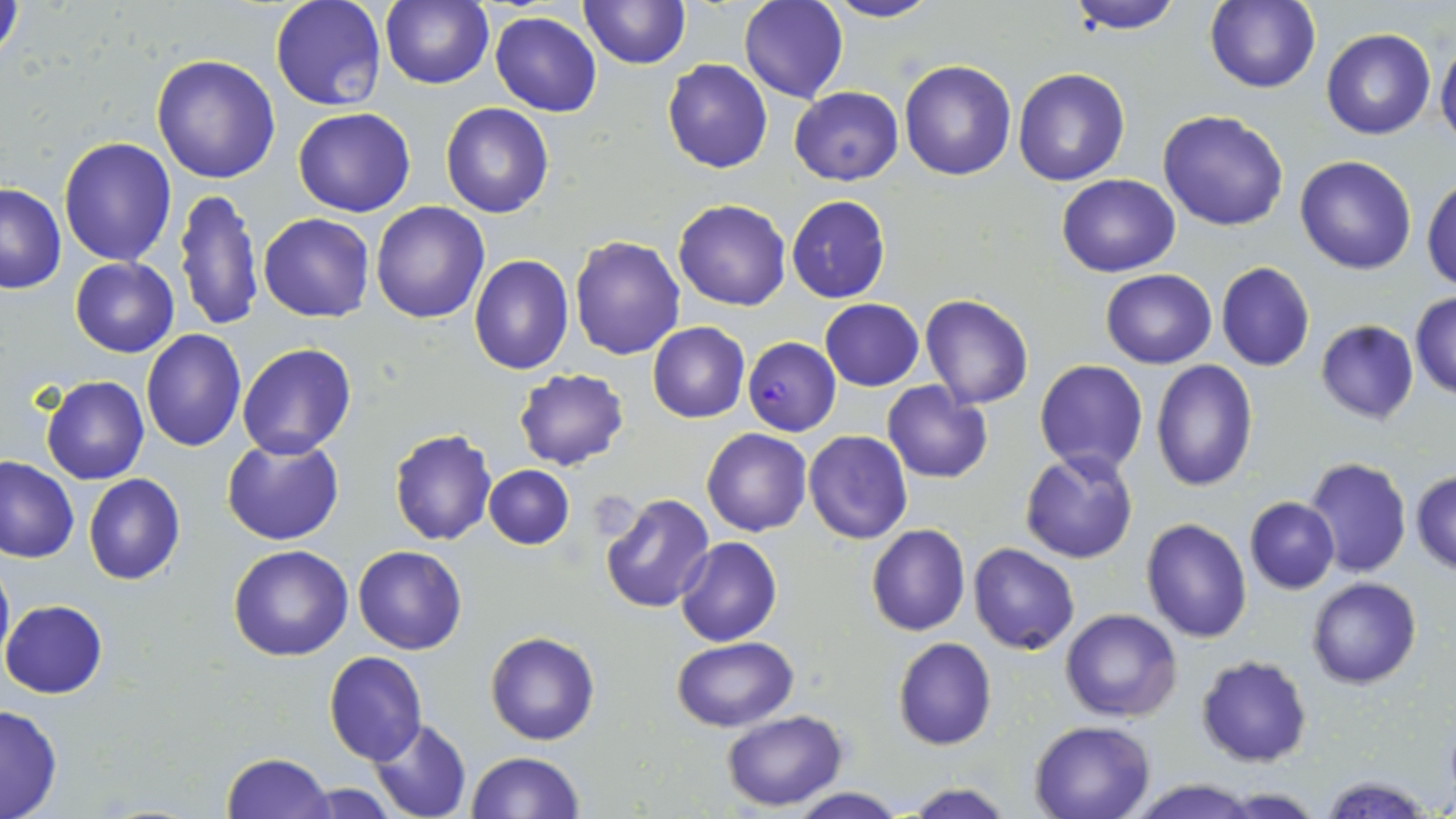
Plasmodium falciparum-infected red blood cell locations = approximate bounding boxes as named x1/y1/x2/y2 corners in pixels: (x1=744, y1=337, x2=842, y2=436)
slide-level diagnosis = Plasmodium falciparum
image size = 1456×819 pixels
field of view = one of a larger specimen
uninfected red blood cell locations = approximate bounding boxes as named x1/y1/x2/y2 corners in pixels: (x1=382, y1=0, x2=494, y2=89), (x1=580, y1=0, x2=691, y2=70), (x1=824, y1=0, x2=940, y2=24), (x1=1064, y1=0, x2=1188, y2=32), (x1=272, y1=1, x2=386, y2=112), (x1=738, y1=1, x2=848, y2=104), (x1=1204, y1=1, x2=1321, y2=93), (x1=1, y1=2, x2=28, y2=68), (x1=491, y1=10, x2=603, y2=117), (x1=1321, y1=29, x2=1435, y2=140), (x1=1435, y1=39, x2=1456, y2=149), (x1=151, y1=55, x2=281, y2=185), (x1=662, y1=58, x2=772, y2=174), (x1=898, y1=60, x2=1017, y2=181), (x1=1013, y1=67, x2=1130, y2=185), (x1=788, y1=86, x2=904, y2=185), (x1=440, y1=102, x2=554, y2=218), (x1=293, y1=105, x2=416, y2=218), (x1=1158, y1=109, x2=1290, y2=231), (x1=59, y1=136, x2=177, y2=266), (x1=1294, y1=155, x2=1417, y2=274), (x1=1056, y1=173, x2=1180, y2=275), (x1=1422, y1=175, x2=1456, y2=291), (x1=0, y1=184, x2=65, y2=294), (x1=174, y1=188, x2=262, y2=331), (x1=786, y1=195, x2=891, y2=303), (x1=673, y1=199, x2=791, y2=311), (x1=371, y1=201, x2=490, y2=323), (x1=259, y1=213, x2=375, y2=322), (x1=570, y1=235, x2=686, y2=359), (x1=469, y1=255, x2=574, y2=374), (x1=70, y1=256, x2=179, y2=357), (x1=1216, y1=262, x2=1315, y2=373), (x1=1101, y1=269, x2=1217, y2=369), (x1=1409, y1=292, x2=1456, y2=399), (x1=920, y1=293, x2=1034, y2=409), (x1=819, y1=299, x2=924, y2=391), (x1=1315, y1=320, x2=1421, y2=425), (x1=647, y1=322, x2=749, y2=422), (x1=140, y1=329, x2=245, y2=450), (x1=237, y1=344, x2=357, y2=459), (x1=1034, y1=359, x2=1148, y2=478), (x1=1150, y1=359, x2=1259, y2=491), (x1=513, y1=367, x2=629, y2=471), (x1=40, y1=374, x2=149, y2=485), (x1=883, y1=381, x2=994, y2=484), (x1=702, y1=427, x2=812, y2=537), (x1=389, y1=430, x2=497, y2=546), (x1=803, y1=430, x2=912, y2=544), (x1=222, y1=437, x2=345, y2=545), (x1=1020, y1=450, x2=1138, y2=564), (x1=1304, y1=456, x2=1411, y2=578), (x1=0, y1=457, x2=79, y2=564), (x1=484, y1=465, x2=573, y2=549), (x1=1410, y1=469, x2=1456, y2=576), (x1=84, y1=473, x2=185, y2=585), (x1=597, y1=491, x2=715, y2=613), (x1=1244, y1=497, x2=1339, y2=593), (x1=1141, y1=517, x2=1252, y2=644), (x1=866, y1=524, x2=971, y2=636), (x1=675, y1=537, x2=783, y2=646), (x1=969, y1=542, x2=1079, y2=655), (x1=352, y1=544, x2=467, y2=654), (x1=227, y1=545, x2=353, y2=662), (x1=0, y1=550, x2=13, y2=674), (x1=1307, y1=576, x2=1423, y2=689), (x1=1, y1=599, x2=108, y2=698), (x1=1061, y1=608, x2=1182, y2=723), (x1=485, y1=631, x2=598, y2=745), (x1=672, y1=637, x2=799, y2=730), (x1=893, y1=638, x2=996, y2=751), (x1=325, y1=651, x2=428, y2=764), (x1=1196, y1=655, x2=1312, y2=767), (x1=1, y1=701, x2=64, y2=819), (x1=722, y1=710, x2=848, y2=811), (x1=369, y1=717, x2=471, y2=819), (x1=1029, y1=720, x2=1155, y2=819), (x1=465, y1=751, x2=582, y2=818), (x1=221, y1=752, x2=334, y2=818), (x1=1322, y1=776, x2=1433, y2=818), (x1=1124, y1=779, x2=1264, y2=818), (x1=900, y1=782, x2=1016, y2=819), (x1=300, y1=783, x2=398, y2=818), (x1=791, y1=789, x2=905, y2=819)
modality = light microscopy
stain = May-Grünwald-Giemsa
magnification = 1000x
preparation = thin blood smear